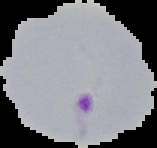
preparation = thin blood film
malaria status = parasitized
image size = 157×148 pixels
image type = segmented cell region with the area outside set to black